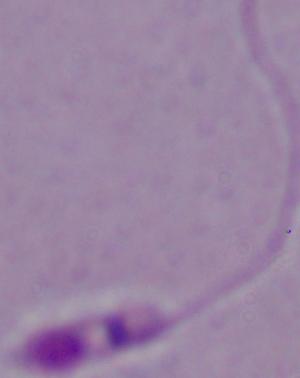

modality = photomicrograph
magnification = 1000x
identification = Leishmania